Describe the morphology of the erythrocytes.
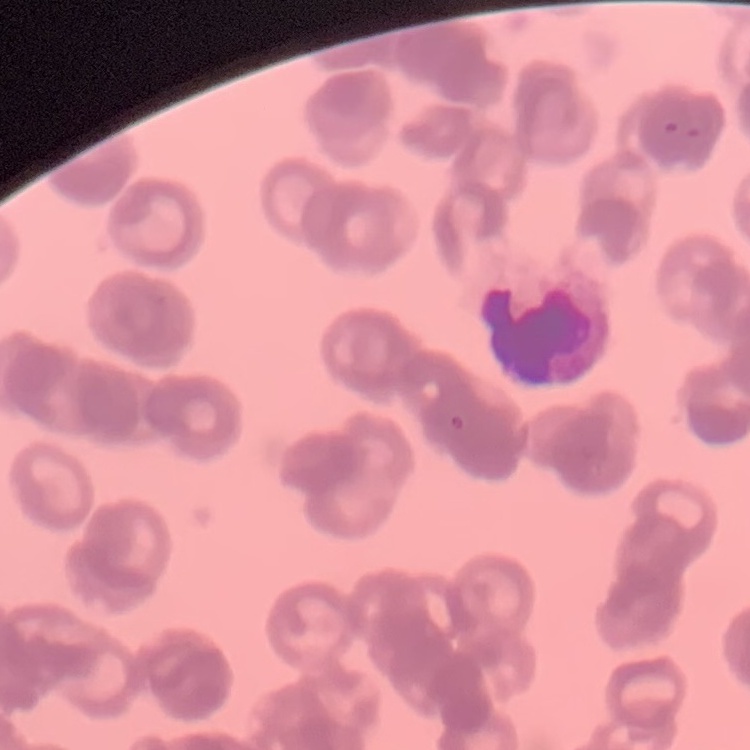

Rouleaux formation.

Thin blood smear. One tile cut from a larger photomicrograph. Stained with either Field's or Giemsa.